Identify the parasite.
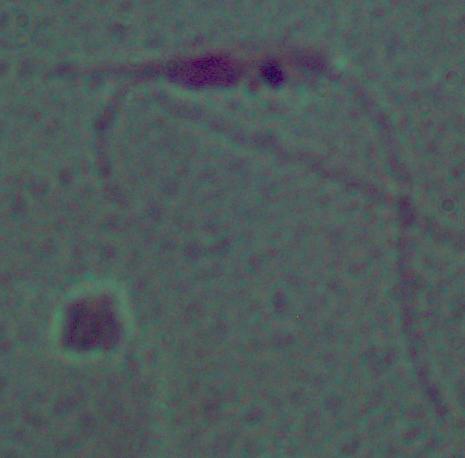
Leishmania.

Photomicrograph. Captured at 1000x magnification.